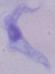
Summary:
  - Modality: photomicrograph
  - Identification: trypanosome
  - Magnification: 1000x